Report the malaria status of this cell.
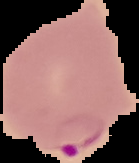

Parasitized.

preparation = thin blood film
image type = segmented cell region on a black background
image size = 139×163 pixels